Assess this cell for malaria.
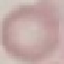

It is uninfected.

Automatically extracted cell patch, resized to 64 × 64 pixels. Giemsa-stained preparation. Thin blood smear. Photographed with a smartphone camera at the microscope eyepiece.